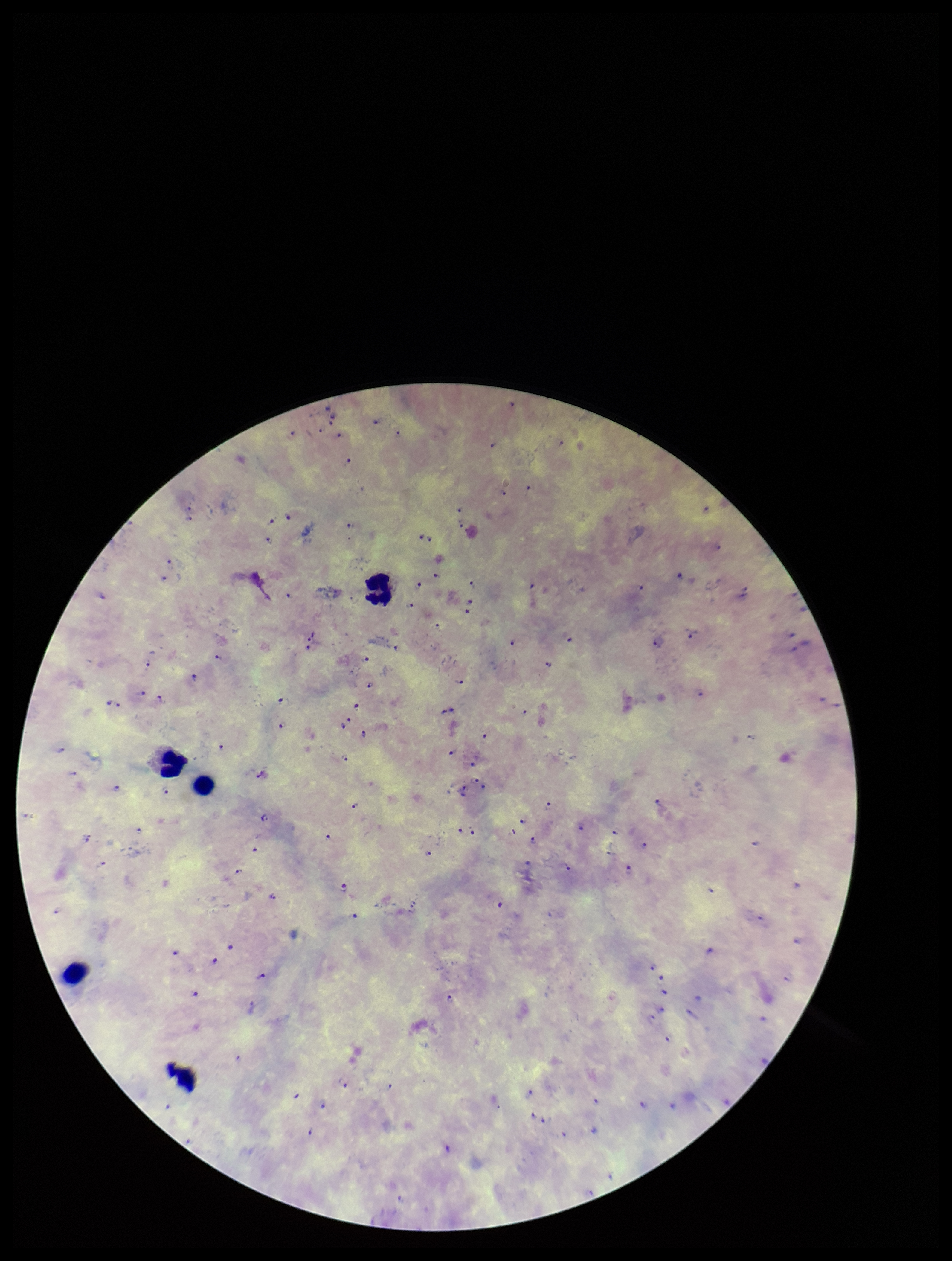
{
  "leukocyte_count": 5,
  "plasmodium_parasites": "seen",
  "patient_malaria_status": "infected",
  "preparation": "thick",
  "capture": "smartphone photograph through the microscope eyepiece",
  "field_of_view": "one from this slide",
  "stain": "Giemsa",
  "species_reported_for_this_patient": "Plasmodium falciparum",
  "image_size": "952×1261 pixels",
  "parasite_count": 101
}